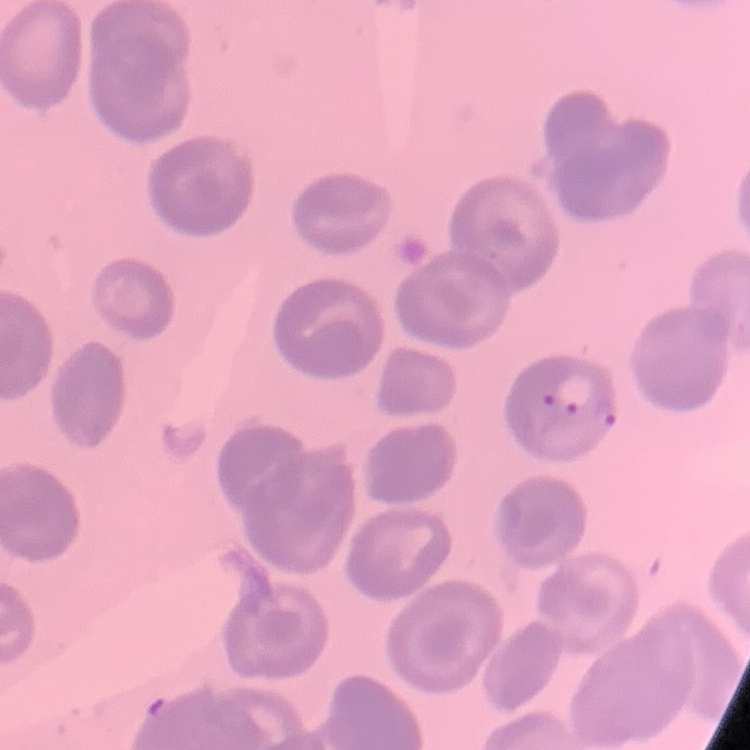

erythrocyte morphology = no rouleaux formation
image type = one tile cut from a larger photomicrograph
preparation = thin peripheral smear
stain = Field's or Giemsa